Give the position of every malaria parasite.
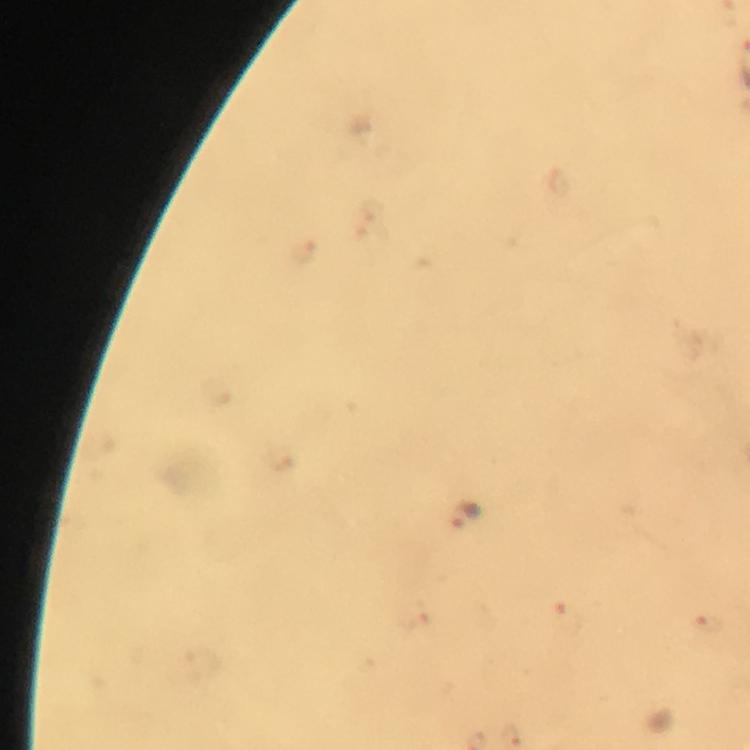
Approximate centers as {x, y} in pixels.
Malaria parasites: {463, 513}.

{
  "cropped_from": "one field of view",
  "magnification": "100x",
  "stain": "Giemsa",
  "capture": "smartphone mounted on the microscope",
  "image_size": "750×750 pixels",
  "context": "from a diagnostic examination for malaria",
  "preparation": "thick blood smear",
  "immersion_oil": "applied"
}